Comment on the morphology of the red blood cells.
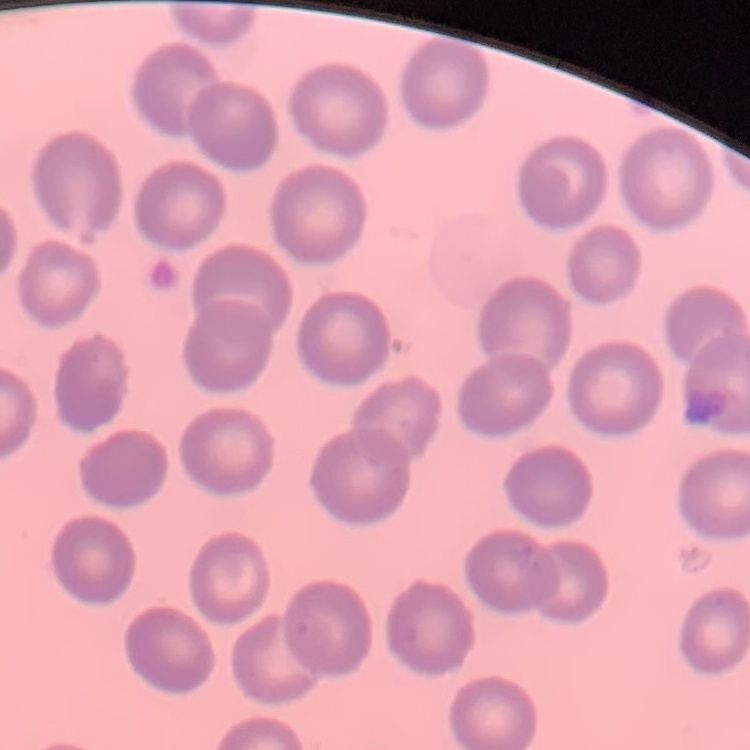

No rouleaux formation.

Square crop of a larger photomicrograph. Stained with either Field's or Giemsa. Thin blood smear.